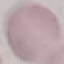

result = no malaria parasites detected
image type = automatically extracted cell patch, resized to 64 × 64 pixels
stain = Giemsa
capture = smartphone through the microscope eyepiece
preparation = thin blood film